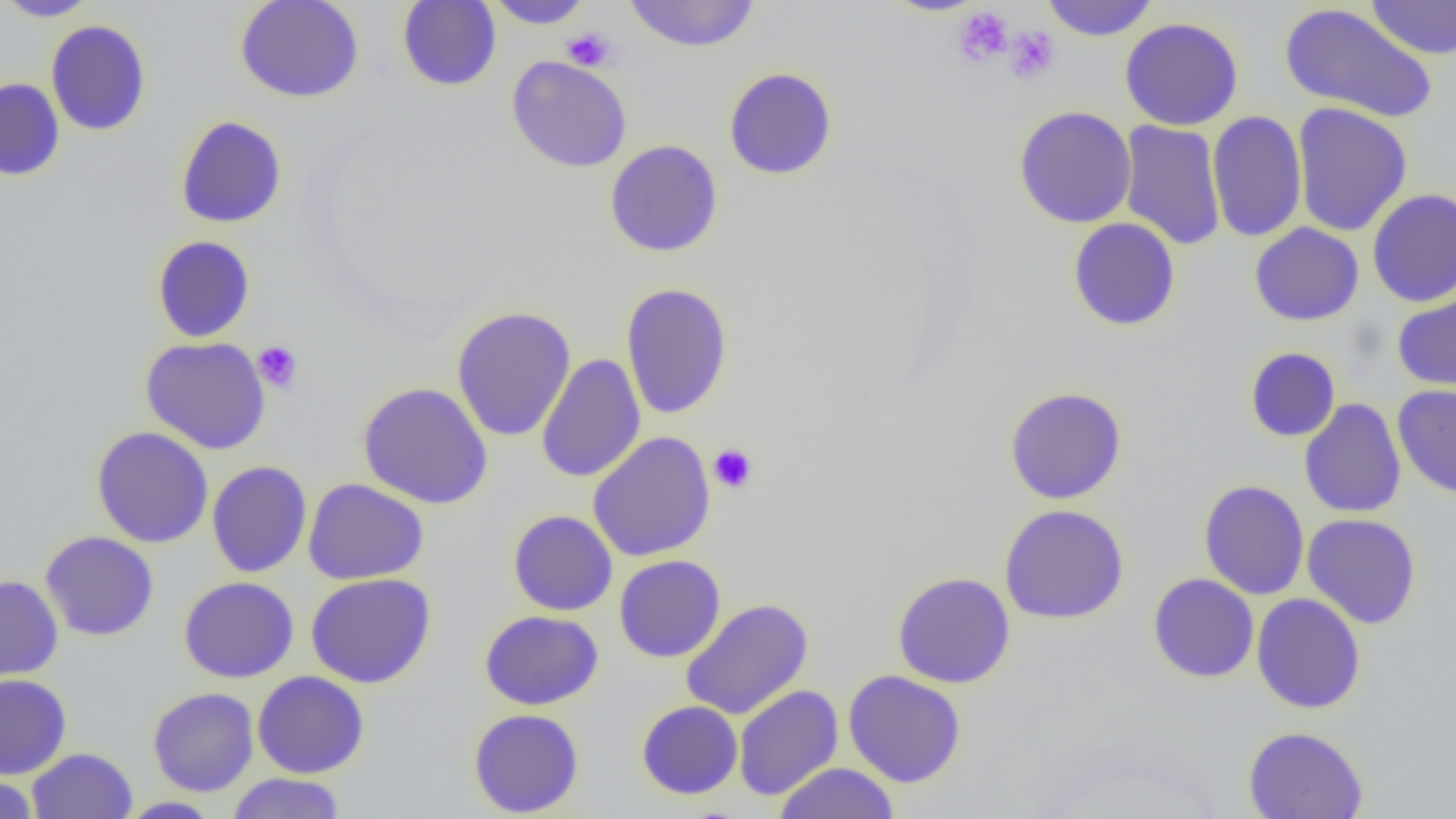
slide-level diagnosis = negative for blood parasites
uninfected red blood cell locations = approximate bounding boxes as (x1,y1)-(x2,y2) corner pairs in pixels: (0,0)-(98,21), (234,0)-(364,103), (397,0)-(501,91), (483,0)-(593,29), (623,0)-(760,52), (880,0)-(990,16), (1041,0)-(1158,41), (1365,0)-(1456,60), (1279,2)-(1438,125), (1119,17)-(1244,131), (46,20)-(151,136), (507,55)-(632,173), (723,66)-(838,180), (0,78)-(65,181), (1292,103)-(1412,236), (1014,106)-(1137,229), (1207,110)-(1307,242), (175,115)-(287,228), (1118,120)-(1226,250), (605,139)-(723,258), (1367,188)-(1456,307), (1067,217)-(1181,332), (1249,223)-(1364,326), (152,236)-(256,343), (620,283)-(734,420), (1392,287)-(1456,394), (451,306)-(576,442), (140,337)-(271,454), (1244,347)-(1341,442), (536,353)-(646,483), (357,381)-(493,509), (1392,384)-(1456,499), (1003,386)-(1127,505), (1299,398)-(1406,518), (91,426)-(214,548), (588,432)-(716,561), (207,461)-(312,578), (303,478)-(429,585), (1198,479)-(1309,600), (999,503)-(1130,625), (508,510)-(618,616), (1302,513)-(1422,629), (40,531)-(159,641), (614,555)-(725,662), (892,571)-(1016,689), (305,573)-(436,688), (1148,573)-(1259,683), (0,575)-(63,681), (178,576)-(299,683), (1251,593)-(1366,714), (680,598)-(814,720), (479,609)-(604,710), (843,670)-(967,788), (252,671)-(369,778), (0,673)-(72,779), (733,685)-(844,801), (148,687)-(259,796), (636,700)-(743,800), (468,708)-(584,817), (1242,726)-(1369,819), (27,747)-(137,819), (774,762)-(900,819), (226,772)-(347,818), (0,774)-(41,819), (116,797)-(225,818)
image size = 1456×819 pixels
magnification = 1000x
platelet locations = approximate bounding boxes as (x1,y1)-(x2,y2) corner pairs in pixels: (952,6)-(1014,68), (1004,25)-(1059,84), (562,27)-(617,71), (252,340)-(303,393), (708,443)-(758,494)
field of view = one of a larger specimen
modality = light microscopy
preparation = thin blood film